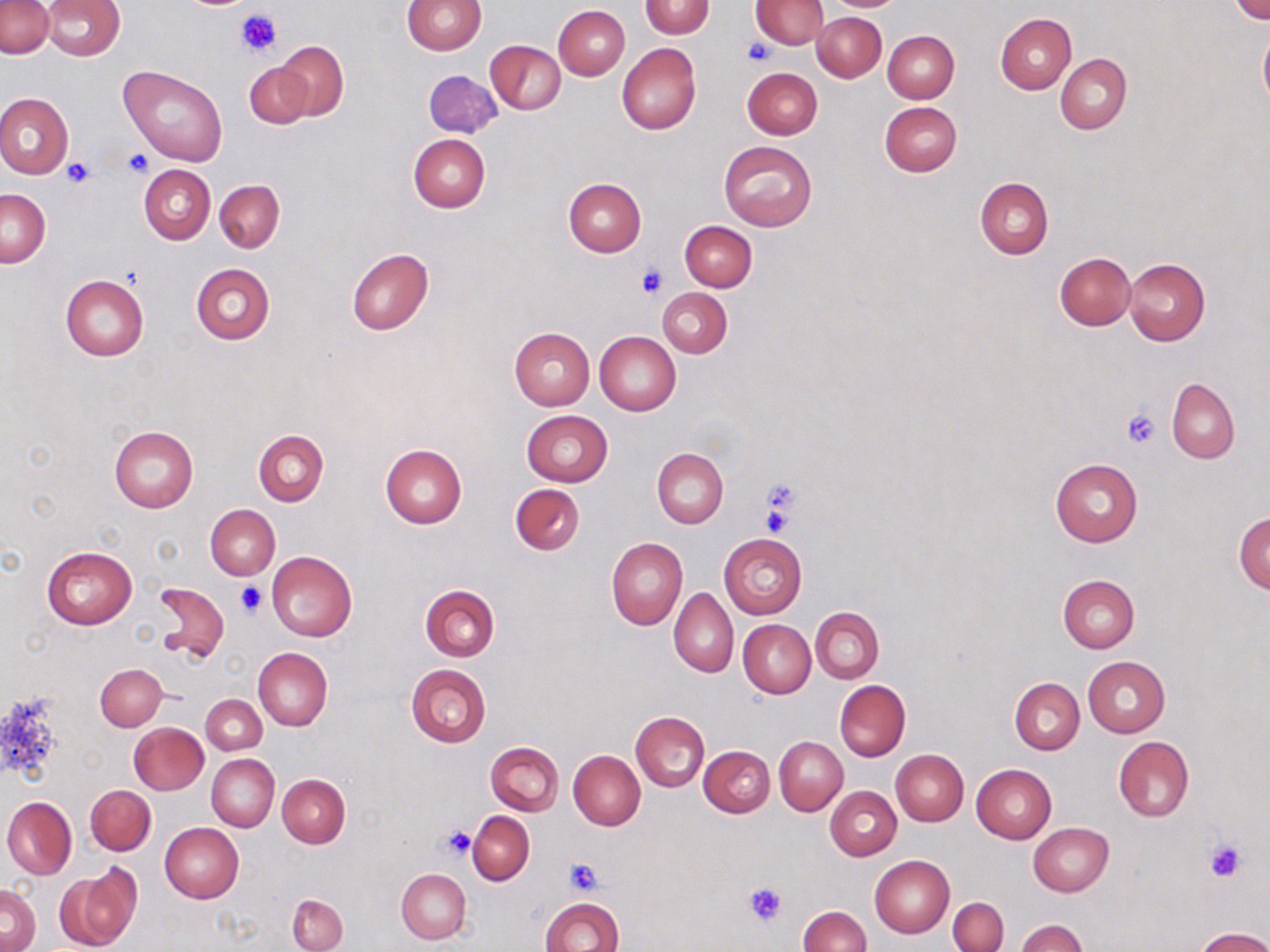
Approximate bounding boxes as named x1/y1/x2/y2 corners in pixels. Platelet locations: (x1=235, y1=7, x2=279, y2=59), (x1=744, y1=37, x2=774, y2=65), (x1=123, y1=148, x2=154, y2=177), (x1=62, y1=158, x2=94, y2=187), (x1=636, y1=265, x2=666, y2=299), (x1=1121, y1=408, x2=1160, y2=449), (x1=757, y1=476, x2=803, y2=533), (x1=235, y1=582, x2=266, y2=616), (x1=441, y1=825, x2=478, y2=860), (x1=1203, y1=838, x2=1246, y2=882), (x1=564, y1=857, x2=606, y2=894), (x1=744, y1=882, x2=785, y2=927). Uninfected red blood cell locations: (x1=1, y1=0, x2=54, y2=58), (x1=401, y1=0, x2=485, y2=55), (x1=640, y1=0, x2=712, y2=39), (x1=751, y1=0, x2=828, y2=49), (x1=829, y1=0, x2=902, y2=11), (x1=1231, y1=0, x2=1268, y2=23), (x1=43, y1=1, x2=125, y2=60), (x1=553, y1=5, x2=630, y2=80), (x1=814, y1=12, x2=886, y2=81), (x1=996, y1=14, x2=1075, y2=93), (x1=1257, y1=28, x2=1270, y2=109), (x1=884, y1=31, x2=959, y2=103), (x1=486, y1=39, x2=566, y2=115), (x1=275, y1=41, x2=349, y2=121), (x1=616, y1=43, x2=701, y2=135), (x1=1055, y1=54, x2=1131, y2=134), (x1=244, y1=61, x2=313, y2=128), (x1=120, y1=66, x2=227, y2=166), (x1=741, y1=67, x2=823, y2=140), (x1=423, y1=70, x2=503, y2=139), (x1=0, y1=92, x2=74, y2=179), (x1=879, y1=101, x2=961, y2=177), (x1=408, y1=133, x2=490, y2=212), (x1=718, y1=140, x2=817, y2=231), (x1=139, y1=165, x2=215, y2=244), (x1=974, y1=177, x2=1052, y2=258), (x1=564, y1=178, x2=646, y2=256), (x1=215, y1=181, x2=285, y2=252), (x1=1, y1=188, x2=50, y2=266), (x1=680, y1=221, x2=757, y2=292), (x1=347, y1=247, x2=433, y2=336), (x1=1055, y1=252, x2=1135, y2=330), (x1=1123, y1=257, x2=1210, y2=346), (x1=191, y1=264, x2=275, y2=345), (x1=61, y1=274, x2=149, y2=362), (x1=657, y1=288, x2=732, y2=358), (x1=509, y1=328, x2=594, y2=410), (x1=594, y1=332, x2=681, y2=415), (x1=1167, y1=378, x2=1238, y2=463), (x1=521, y1=410, x2=613, y2=487), (x1=515, y1=414, x2=591, y2=554), (x1=110, y1=427, x2=198, y2=512), (x1=254, y1=430, x2=328, y2=506), (x1=380, y1=444, x2=467, y2=529), (x1=652, y1=448, x2=728, y2=528), (x1=1050, y1=459, x2=1143, y2=547), (x1=510, y1=484, x2=585, y2=556), (x1=205, y1=505, x2=280, y2=578), (x1=1234, y1=511, x2=1270, y2=593), (x1=719, y1=533, x2=807, y2=619), (x1=606, y1=537, x2=687, y2=630), (x1=41, y1=546, x2=137, y2=629), (x1=266, y1=551, x2=358, y2=642), (x1=1058, y1=574, x2=1140, y2=652), (x1=151, y1=581, x2=229, y2=662), (x1=419, y1=585, x2=499, y2=661), (x1=669, y1=589, x2=739, y2=676), (x1=811, y1=608, x2=884, y2=682), (x1=738, y1=620, x2=815, y2=698), (x1=253, y1=647, x2=332, y2=731), (x1=1083, y1=656, x2=1170, y2=737), (x1=95, y1=663, x2=167, y2=730), (x1=405, y1=663, x2=491, y2=748), (x1=1009, y1=679, x2=1084, y2=754), (x1=834, y1=680, x2=910, y2=762), (x1=201, y1=694, x2=267, y2=755), (x1=631, y1=711, x2=710, y2=791), (x1=129, y1=723, x2=207, y2=794), (x1=775, y1=736, x2=848, y2=815), (x1=1114, y1=736, x2=1194, y2=820), (x1=485, y1=741, x2=563, y2=815), (x1=699, y1=746, x2=775, y2=817), (x1=891, y1=749, x2=969, y2=826), (x1=568, y1=750, x2=646, y2=829), (x1=207, y1=754, x2=279, y2=831), (x1=970, y1=764, x2=1056, y2=843), (x1=276, y1=775, x2=350, y2=848), (x1=85, y1=785, x2=156, y2=855), (x1=825, y1=786, x2=901, y2=860), (x1=2, y1=796, x2=76, y2=880), (x1=467, y1=811, x2=535, y2=884), (x1=1028, y1=822, x2=1114, y2=896), (x1=160, y1=823, x2=243, y2=903), (x1=869, y1=854, x2=955, y2=938), (x1=55, y1=865, x2=139, y2=952), (x1=397, y1=869, x2=470, y2=944), (x1=1, y1=883, x2=39, y2=952), (x1=286, y1=894, x2=347, y2=952), (x1=540, y1=897, x2=623, y2=952), (x1=948, y1=897, x2=1008, y2=952), (x1=798, y1=906, x2=871, y2=952), (x1=1014, y1=919, x2=1088, y2=952), (x1=1196, y1=927, x2=1270, y2=952). Slide-level diagnosis: no evidence of blood parasites. Thin blood film. Single field of view. Image is 1270×952 pixels. May-Grünwald-Giemsa-stained preparation. 1000x magnification. Light microscopy.